Name the blood parasite species.
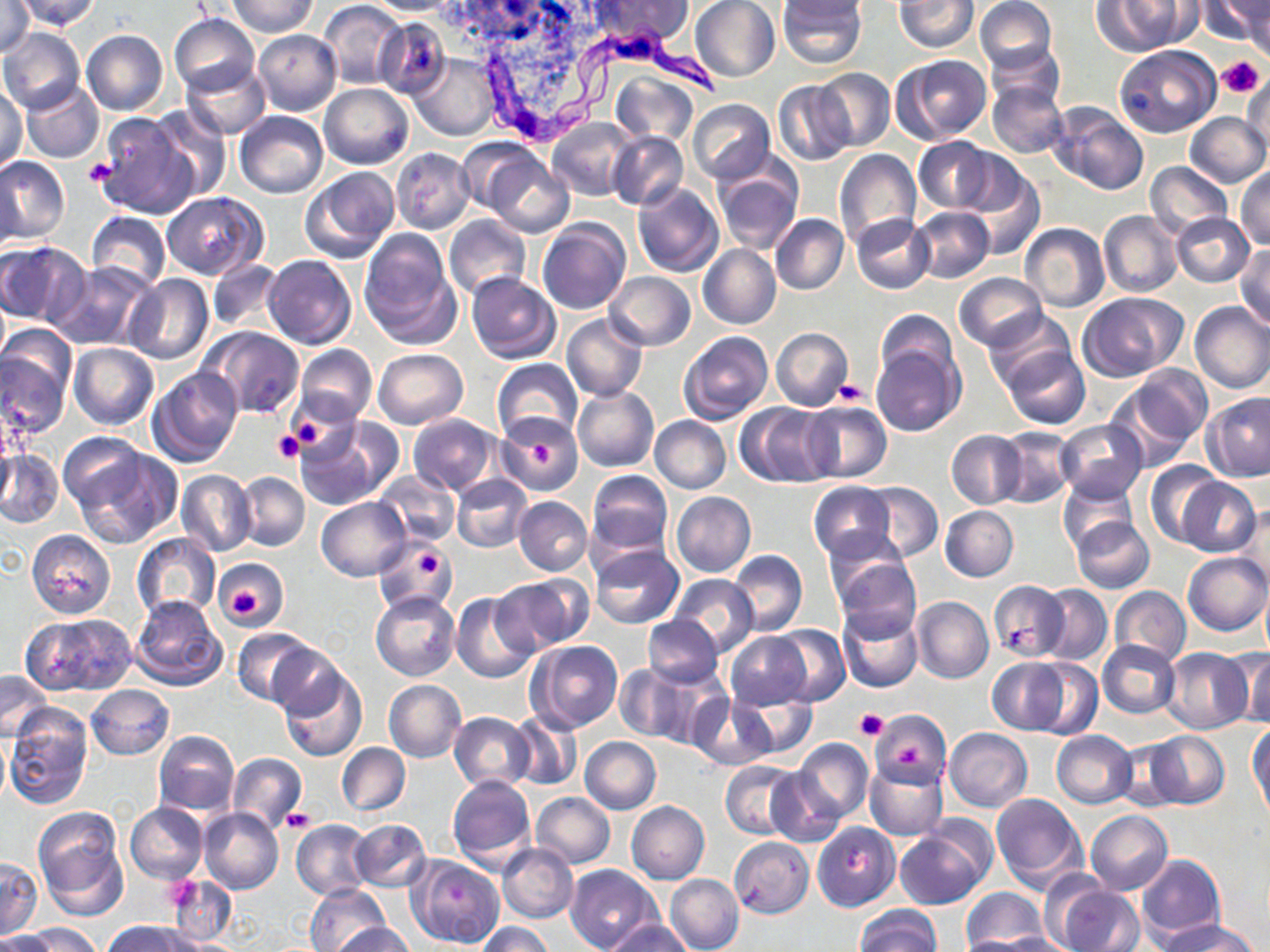
Trypanosoma brucei.

image size = 1270×952 pixels
magnification = 1000x
uninfected red blood cell locations = approximate bounding boxes as [x1, y1, x2, y2] in pixels: [13, 0, 101, 30], [226, 0, 318, 37], [318, 0, 407, 89], [365, 0, 465, 16], [585, 0, 694, 47], [689, 0, 780, 83], [777, 0, 866, 70], [895, 0, 979, 52], [975, 0, 1057, 72], [1199, 0, 1270, 47], [1241, 0, 1270, 61], [1091, 1, 1190, 55], [1, 4, 37, 57], [169, 13, 259, 95], [374, 16, 451, 100], [0, 27, 86, 115], [253, 29, 341, 116], [80, 30, 168, 117], [984, 42, 1066, 115], [1115, 45, 1221, 137], [411, 53, 499, 140], [896, 54, 991, 144], [181, 61, 270, 139], [814, 68, 895, 151], [610, 71, 697, 145], [1242, 74, 1269, 154], [772, 79, 855, 167], [19, 80, 104, 164], [988, 83, 1068, 159], [0, 84, 27, 173], [319, 84, 413, 169], [687, 99, 775, 183], [1048, 101, 1148, 197], [149, 106, 231, 202], [234, 111, 328, 198], [92, 112, 198, 218], [1186, 112, 1268, 188], [1156, 118, 1252, 224], [548, 119, 636, 199], [607, 130, 688, 211], [914, 136, 993, 213], [457, 138, 543, 213], [392, 148, 475, 233], [834, 149, 922, 249], [485, 154, 573, 238], [0, 155, 70, 244], [1146, 162, 1232, 239], [2, 164, 23, 258], [713, 164, 802, 254], [960, 164, 1043, 257], [301, 166, 398, 263], [1235, 168, 1270, 250], [632, 182, 724, 277], [161, 192, 266, 278], [910, 207, 993, 283], [1099, 209, 1182, 298], [86, 211, 171, 292], [1170, 212, 1254, 287], [771, 214, 849, 294], [851, 214, 934, 293], [445, 216, 530, 300], [538, 219, 630, 314], [1020, 223, 1108, 311], [358, 230, 459, 345], [0, 243, 87, 327], [698, 244, 781, 330], [1234, 245, 1270, 328], [263, 254, 357, 349], [206, 259, 284, 332], [49, 260, 157, 351], [604, 271, 696, 351], [956, 272, 1048, 351], [466, 273, 561, 364], [122, 275, 213, 366], [0, 291, 10, 369], [1080, 292, 1187, 381], [1189, 301, 1270, 393], [874, 309, 960, 387], [983, 310, 1075, 393], [562, 313, 648, 401], [200, 326, 304, 417], [772, 327, 853, 411], [678, 330, 773, 424], [0, 340, 72, 439], [69, 342, 159, 429], [296, 345, 377, 424], [871, 345, 964, 437], [1000, 346, 1089, 429], [373, 348, 468, 429], [492, 358, 582, 440], [1115, 365, 1212, 460], [148, 367, 243, 468], [572, 384, 658, 472], [1202, 391, 1270, 481], [801, 400, 892, 483], [735, 402, 833, 487], [407, 413, 498, 496], [495, 413, 585, 497], [649, 416, 731, 493], [294, 419, 394, 511], [1055, 419, 1146, 501], [995, 426, 1077, 510], [946, 430, 1026, 509], [63, 443, 180, 550], [0, 449, 63, 528], [1146, 461, 1223, 546], [374, 469, 460, 546], [176, 470, 256, 556], [586, 470, 673, 557], [236, 472, 309, 551], [451, 473, 533, 553], [1178, 477, 1260, 557], [1059, 479, 1138, 556], [862, 481, 942, 563], [807, 482, 895, 562], [452, 486, 591, 564], [671, 492, 756, 578], [513, 496, 592, 576], [316, 497, 410, 580], [1234, 503, 1269, 597], [940, 506, 1019, 581], [1071, 516, 1154, 594], [822, 528, 914, 610], [26, 530, 116, 620], [132, 533, 220, 620], [374, 536, 455, 615], [590, 542, 684, 628], [728, 549, 808, 636], [1183, 552, 1269, 635], [212, 556, 288, 629], [831, 556, 920, 641], [501, 574, 593, 652], [670, 575, 758, 656], [987, 580, 1070, 662], [1259, 583, 1270, 660], [1036, 585, 1112, 665], [1110, 586, 1191, 666], [371, 592, 460, 681], [451, 592, 538, 683], [130, 595, 227, 691], [912, 596, 994, 683], [837, 605, 923, 693], [26, 612, 137, 696], [642, 614, 723, 686], [769, 624, 850, 706], [231, 628, 317, 706], [724, 633, 811, 710], [1073, 637, 1172, 770], [528, 639, 623, 731], [1097, 640, 1180, 718], [266, 641, 349, 721], [1160, 648, 1253, 734], [1237, 650, 1267, 728], [987, 657, 1070, 734], [1028, 659, 1101, 739], [614, 664, 696, 743], [278, 667, 367, 762], [1, 670, 53, 741], [382, 679, 465, 763], [86, 685, 175, 760], [733, 687, 818, 760], [689, 693, 777, 769], [6, 705, 94, 810], [869, 708, 951, 786], [449, 711, 536, 792], [509, 712, 581, 790], [1249, 723, 1270, 816], [944, 727, 1033, 812], [153, 730, 239, 815], [1051, 730, 1137, 808], [1144, 730, 1229, 809], [0, 732, 10, 807], [581, 737, 661, 814], [792, 737, 873, 824], [1111, 739, 1187, 809], [337, 742, 409, 815], [227, 753, 306, 833], [864, 760, 948, 841], [721, 761, 804, 840], [765, 767, 844, 846], [447, 776, 536, 870], [532, 792, 615, 868], [989, 792, 1085, 890], [625, 801, 710, 884], [126, 803, 207, 883], [200, 808, 284, 894], [34, 811, 127, 917], [1086, 811, 1173, 894], [291, 819, 373, 900], [350, 819, 431, 892], [812, 822, 900, 911], [894, 825, 992, 910], [728, 837, 815, 918], [497, 842, 579, 924], [1136, 854, 1225, 947], [409, 855, 503, 947], [0, 858, 43, 938], [565, 864, 662, 952], [665, 873, 744, 952], [1043, 874, 1141, 952], [169, 875, 236, 945], [305, 883, 390, 952], [962, 887, 1048, 951], [854, 905, 940, 952], [1153, 917, 1258, 952], [604, 918, 692, 952], [104, 920, 194, 952], [477, 922, 554, 952], [24, 923, 101, 952], [333, 923, 418, 952], [1, 930, 56, 952], [983, 933, 1071, 952]
field of view = single
Trypanosoma brucei locations = approximate bounding boxes as [x1, y1, x2, y2] in pixels: [481, 21, 724, 146]
platelet locations = approximate bounding boxes as [x1, y1, x2, y2] in pixels: [1216, 55, 1266, 97], [84, 156, 116, 186], [833, 381, 868, 407], [286, 407, 340, 456], [273, 430, 303, 464], [527, 439, 554, 468], [417, 554, 441, 575], [230, 586, 265, 619], [854, 709, 888, 741], [899, 744, 923, 767], [283, 809, 313, 833]
modality = light microscopy
stain = May-Grünwald-Giemsa
preparation = thin blood film